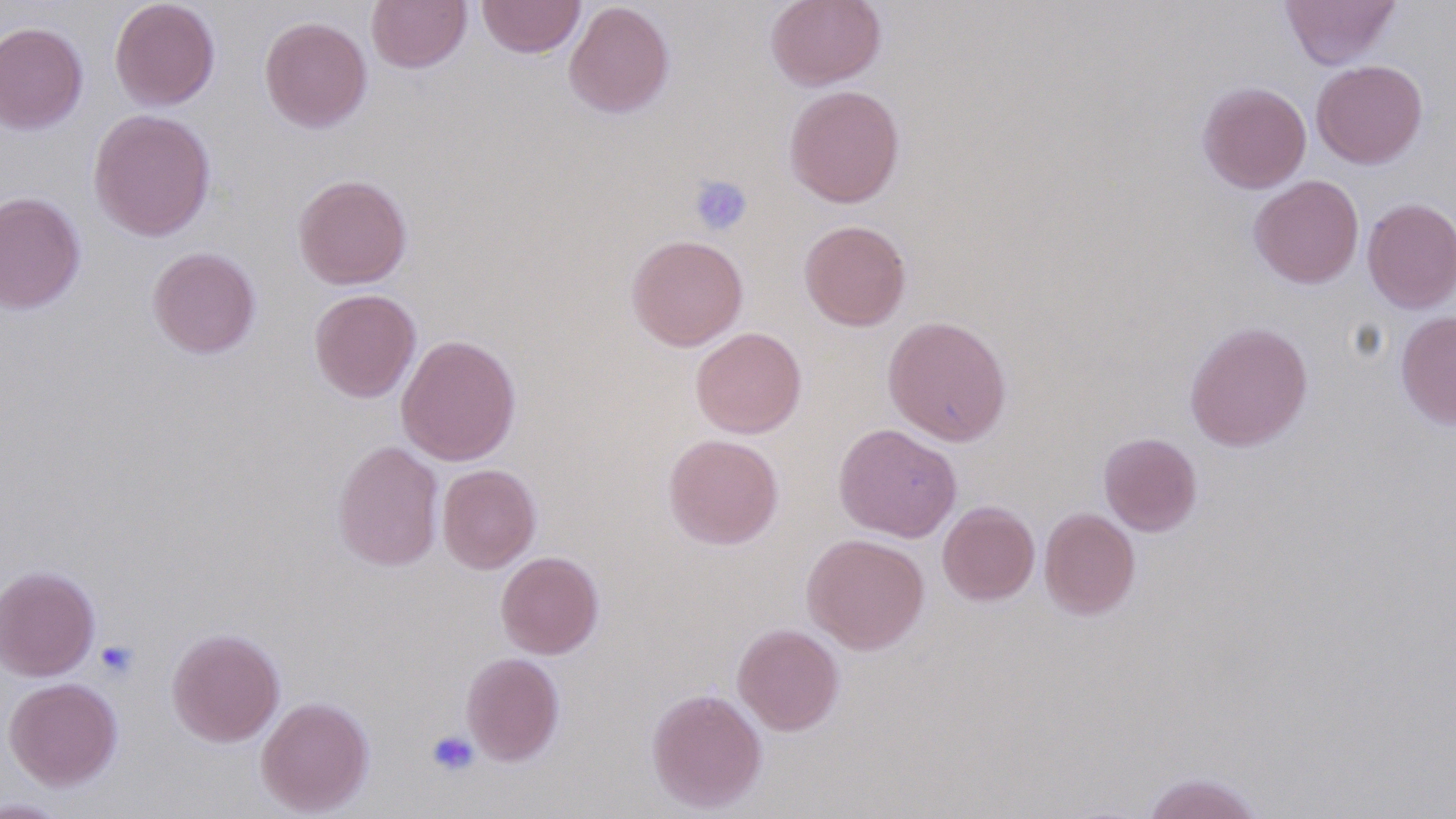
Approximate bounding boxes as (x1, y1, x2, y2) in pixels. Platelet locations: (688, 174, 753, 236), (95, 640, 139, 680), (427, 729, 479, 777). Uninfected red blood cell locations: (109, 0, 221, 111), (366, 0, 472, 73), (477, 0, 585, 58), (765, 0, 886, 90), (1280, 0, 1401, 69), (564, 1, 675, 118), (259, 16, 372, 132), (0, 21, 88, 134), (1311, 59, 1428, 169), (1198, 81, 1312, 193), (784, 84, 905, 208), (89, 108, 216, 242), (293, 173, 412, 289), (1248, 175, 1364, 288), (0, 191, 86, 315), (1362, 198, 1456, 313), (799, 219, 911, 331), (626, 234, 748, 351), (147, 246, 261, 358), (309, 288, 421, 403), (1395, 310, 1456, 430), (883, 315, 1012, 445), (1184, 321, 1313, 451), (690, 327, 807, 438), (396, 334, 522, 466), (834, 423, 962, 542), (1098, 432, 1202, 536), (663, 433, 784, 550), (332, 440, 444, 571), (437, 464, 541, 573), (937, 500, 1040, 606), (1039, 508, 1140, 619), (802, 533, 930, 654), (496, 551, 604, 659), (0, 565, 100, 681), (732, 623, 844, 735), (167, 627, 285, 746), (461, 652, 565, 765), (3, 677, 123, 790), (646, 687, 767, 813), (256, 695, 375, 816), (1139, 771, 1267, 819), (0, 797, 74, 818). Slide-level diagnosis: no evidence of blood parasites. Optical microscopy. 1000x magnification. Single field of view. Image is 1456×819 pixels. Thin blood smear.